Identify the blood parasite species.
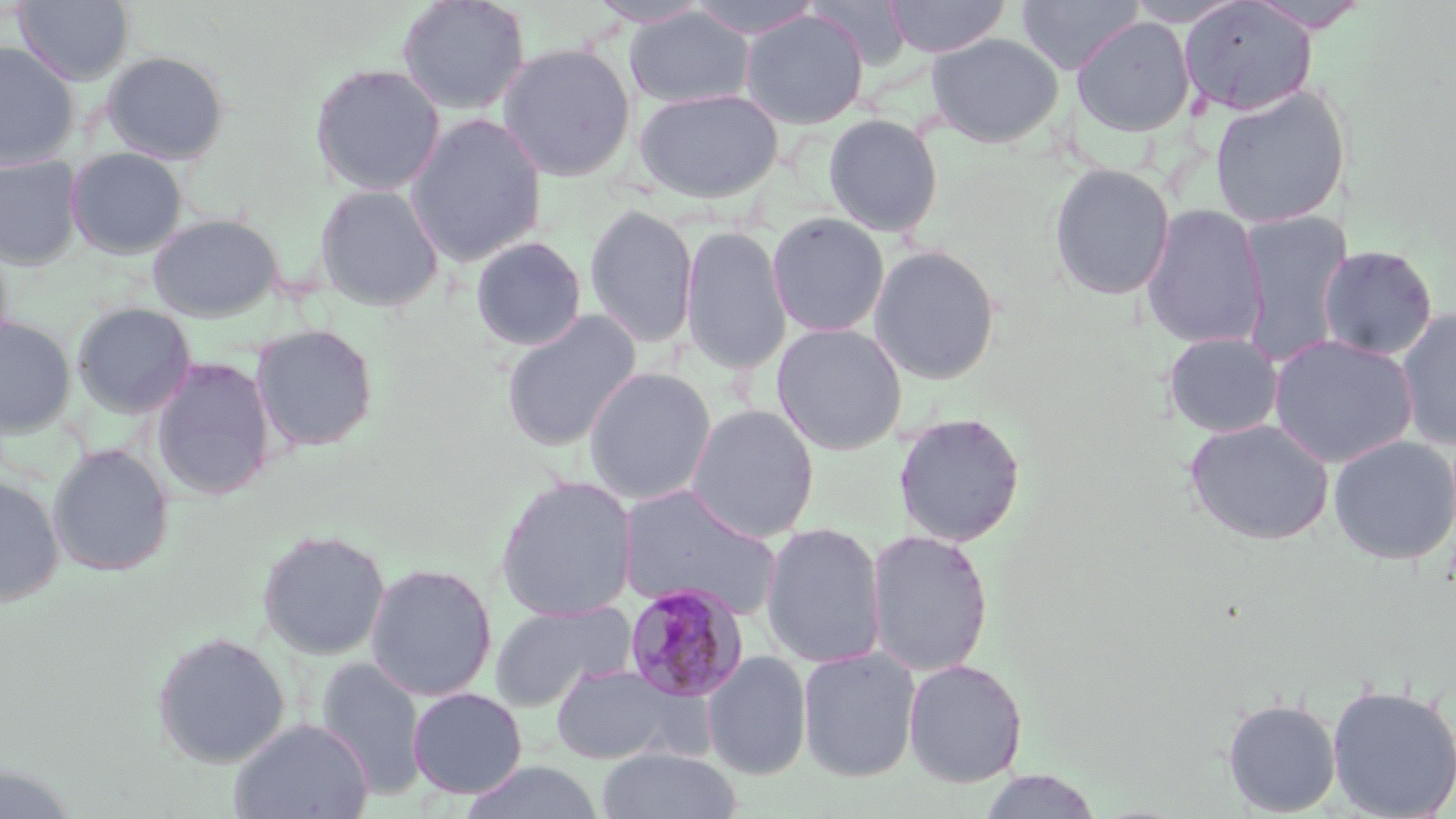
Plasmodium malariae.

Summary:
  - Coordinate format: approximate bounding boxes as (x1,y1)-(x2,y2) corner pairs in pixels
  - Uninfected red blood cell locations: (13,0)-(134,84), (397,0)-(530,115), (685,0)-(825,40), (807,0)-(914,70), (883,0)-(1010,58), (1016,0)-(1144,75), (1180,0)-(1318,117), (587,1)-(712,28), (625,7)-(755,109), (739,10)-(869,129), (1071,15)-(1196,137), (926,32)-(1064,148), (0,42)-(79,170), (496,43)-(636,181), (101,50)-(229,165), (309,62)-(446,196), (1208,85)-(1349,229), (633,88)-(784,204), (406,113)-(547,267), (823,113)-(944,237), (65,147)-(188,259), (0,155)-(84,271), (1048,163)-(1176,301), (313,182)-(445,313), (584,203)-(699,349), (1140,203)-(1268,350), (1236,211)-(1352,365), (767,212)-(889,337), (147,213)-(284,321), (680,225)-(792,376), (0,231)-(14,359), (470,236)-(587,352), (868,244)-(1002,385), (1316,244)-(1438,360), (71,302)-(196,419), (1395,307)-(1456,452), (500,310)-(642,452), (0,317)-(76,437), (251,323)-(379,452), (771,323)-(908,455), (1162,331)-(1284,438), (1268,334)-(1419,467), (150,356)-(276,500), (583,367)-(717,505), (685,404)-(820,542), (893,411)-(1026,546), (1183,418)-(1334,546), (1328,435)-(1456,566), (47,443)-(174,576), (0,475)-(65,606), (494,476)-(638,621), (617,484)-(784,622), (760,522)-(886,669), (865,528)-(994,678), (257,529)-(390,660), (365,562)-(498,702), (490,600)-(637,710), (151,631)-(290,768), (797,645)-(921,783), (702,650)-(812,780), (315,656)-(428,801), (903,658)-(1028,787), (549,663)-(688,766), (1326,683)-(1455,819), (407,687)-(528,798), (1221,697)-(1342,817), (229,718)-(375,819), (596,746)-(742,819), (458,761)-(607,819), (0,764)-(78,819), (976,770)-(1104,818)
  - Plasmodium malariae-infected red blood cell locations: (623,583)-(748,703)
  - Field of view: one of a larger specimen
  - Preparation: thin blood smear
  - Image size: 1456×819 pixels
  - Magnification: 1000x
  - Modality: light microscopy
  - Stain: May-Grünwald-Giemsa